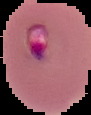
preparation: thin blood smear
image_size: 91×115 pixels
result: Plasmodium parasites detected
image_type: segmented cell region on a black background